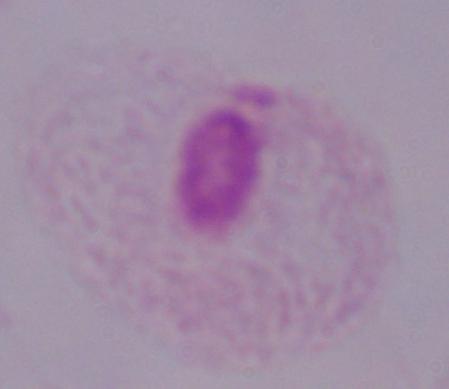

magnification = 1000x
modality = micrograph
identification = trichomonad